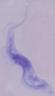
Summary:
  - Modality: micrograph
  - Identification: trypanosome
  - Magnification: 1000x